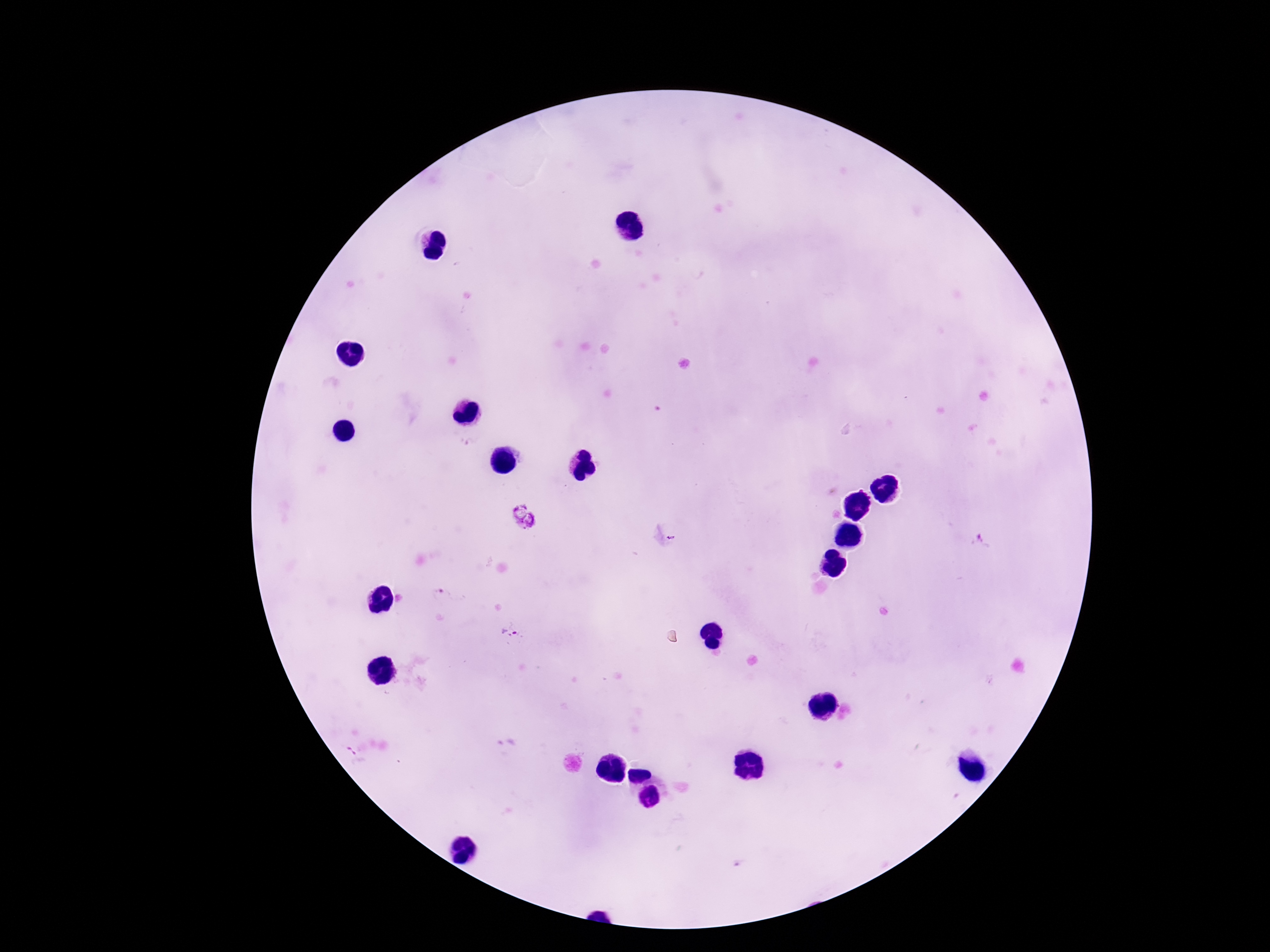
Approximate centers as [x, y] in pixels. Plasmodium parasite locations: [523, 516], [982, 541], [438, 592], [511, 632]. Giemsa-stained preparation. Patient malaria status: infected. Thick peripheral-blood smear. One field from this slide. Image is 1270×952 pixels. 100x magnification. Photographed through the microscope eyepiece with a smartphone camera.